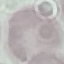

result = no malaria parasites seen
preparation = thin blood smear
image type = cell patch, automatically extracted from a larger field of view and resized to 64 × 64 pixels
capture = smartphone camera at the microscope eyepiece
stain = Giemsa